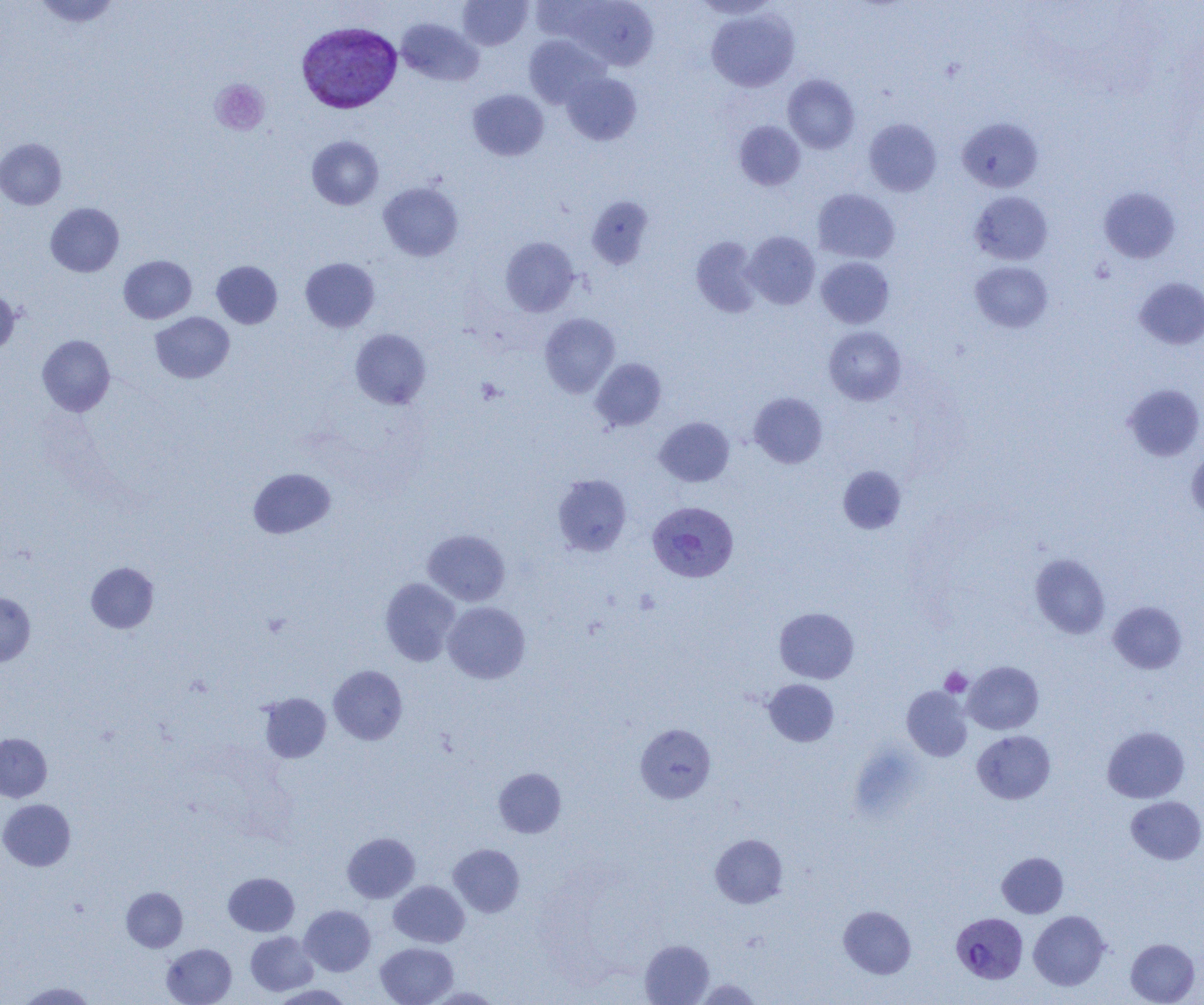
slide-level diagnosis = Plasmodium vivax
uninfected red blood cell locations = approximate bounding boxes as (x1, y1, x2, y2) in pixels: (31, 0, 123, 29), (458, 0, 532, 50), (562, 1, 658, 70), (707, 9, 799, 91), (396, 18, 483, 86), (524, 35, 608, 108), (561, 72, 641, 145), (783, 74, 860, 153), (468, 89, 548, 160), (957, 117, 1043, 192), (864, 118, 941, 196), (734, 120, 805, 191), (307, 136, 384, 210), (0, 138, 66, 209), (378, 181, 463, 262), (1099, 187, 1180, 263), (812, 188, 900, 263), (970, 191, 1052, 265), (586, 197, 654, 269), (45, 202, 124, 277), (743, 231, 820, 309), (690, 236, 762, 317), (501, 237, 579, 316), (118, 255, 197, 323), (300, 257, 380, 332), (816, 257, 894, 329), (211, 260, 282, 328), (970, 261, 1053, 332), (1134, 277, 1204, 349), (0, 288, 21, 357), (150, 312, 235, 383), (540, 313, 620, 397), (824, 326, 906, 405), (350, 329, 431, 409), (37, 335, 115, 416), (591, 358, 666, 431), (1123, 383, 1204, 461), (749, 392, 827, 468), (654, 417, 734, 487), (1186, 448, 1204, 520), (837, 466, 906, 534), (248, 468, 335, 538), (553, 475, 631, 556), (423, 529, 510, 606), (1030, 554, 1110, 639), (86, 562, 158, 633), (379, 577, 460, 666), (0, 593, 35, 666), (442, 601, 530, 684), (1108, 601, 1187, 674), (774, 607, 859, 683), (963, 661, 1043, 734), (328, 665, 407, 744), (764, 679, 839, 747), (902, 686, 972, 761), (259, 693, 331, 763), (635, 724, 716, 803), (1102, 726, 1190, 803), (972, 730, 1056, 804), (0, 733, 52, 802), (493, 768, 566, 837), (1126, 796, 1204, 864), (0, 799, 75, 871), (342, 832, 420, 903), (711, 834, 787, 908), (448, 844, 525, 917), (997, 852, 1068, 918), (223, 872, 299, 936), (389, 880, 469, 948), (121, 887, 187, 952), (300, 905, 375, 976), (839, 905, 916, 978), (1028, 910, 1110, 990), (245, 931, 318, 996), (640, 939, 714, 1005), (1126, 939, 1199, 1005), (375, 942, 458, 1005), (162, 943, 236, 1005), (696, 979, 762, 1004), (16, 981, 96, 1004), (269, 984, 354, 1004), (425, 986, 503, 1004)
magnification = 1000x
modality = light microscopy
field of view = single
Plasmodium vivax-infected red blood cell locations = approximate bounding boxes as (x1, y1, x2, y2) in pixels: (297, 22, 402, 113), (647, 501, 738, 581), (951, 912, 1028, 984)
platelet locations = approximate bounding boxes as (x1, y1, x2, y2) in pixels: (210, 79, 270, 136), (476, 377, 505, 404), (939, 667, 972, 697)
image size = 1204×1005 pixels
preparation = thin blood smear